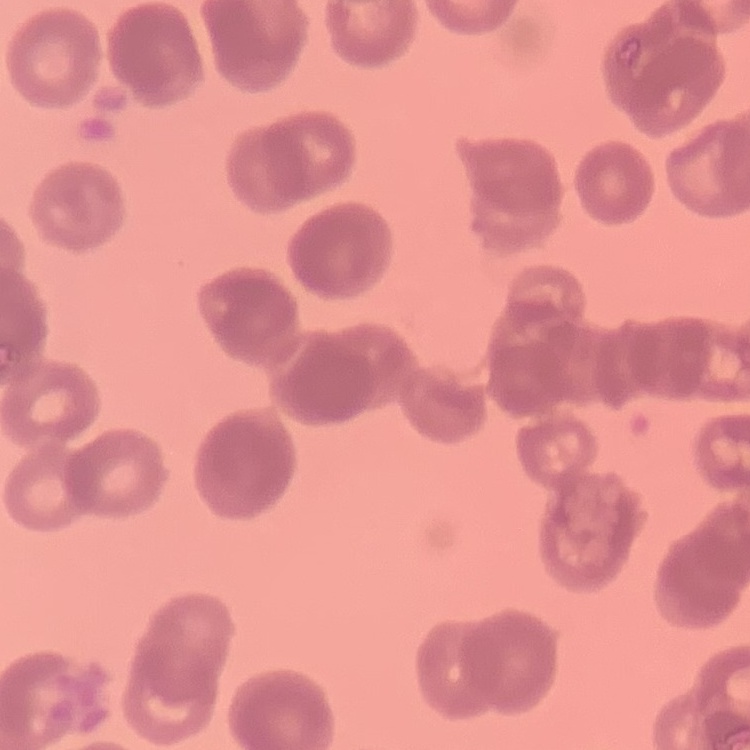
Summary:
  - Red blood cell morphology: rouleaux formation
  - Image type: one tile cut from a larger photomicrograph
  - Stain: Field's or Giemsa
  - Preparation: thin blood film